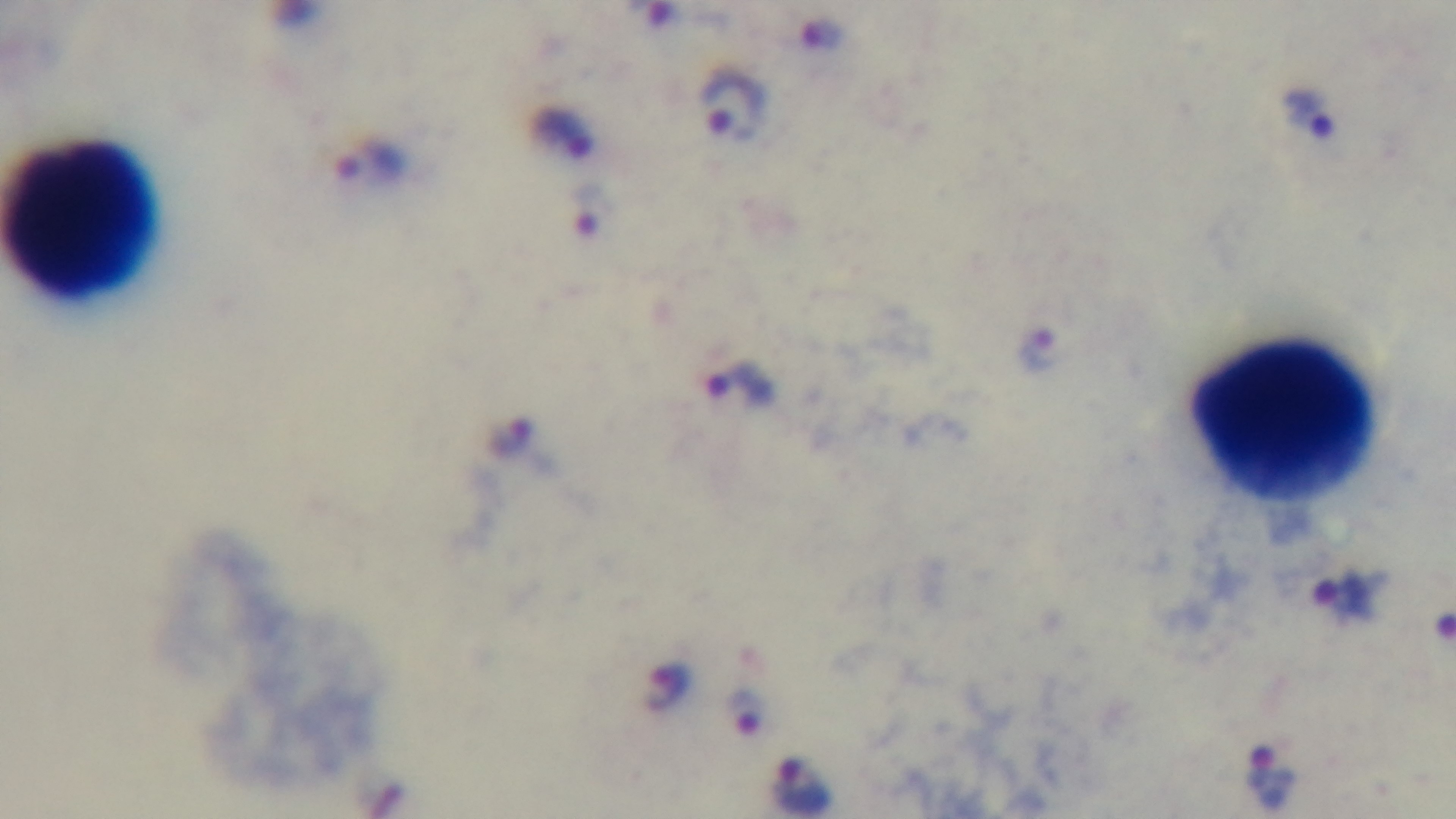

Summary:
  - Field of view: single
  - Capture: mounted 4K digital camera
  - Objective: 100x oil immersion
  - Stain: Giemsa
  - Modality: light microscopy
  - Preparation: thick smear
  - Malaria status: positive